Outline each blood parasite and name the species.
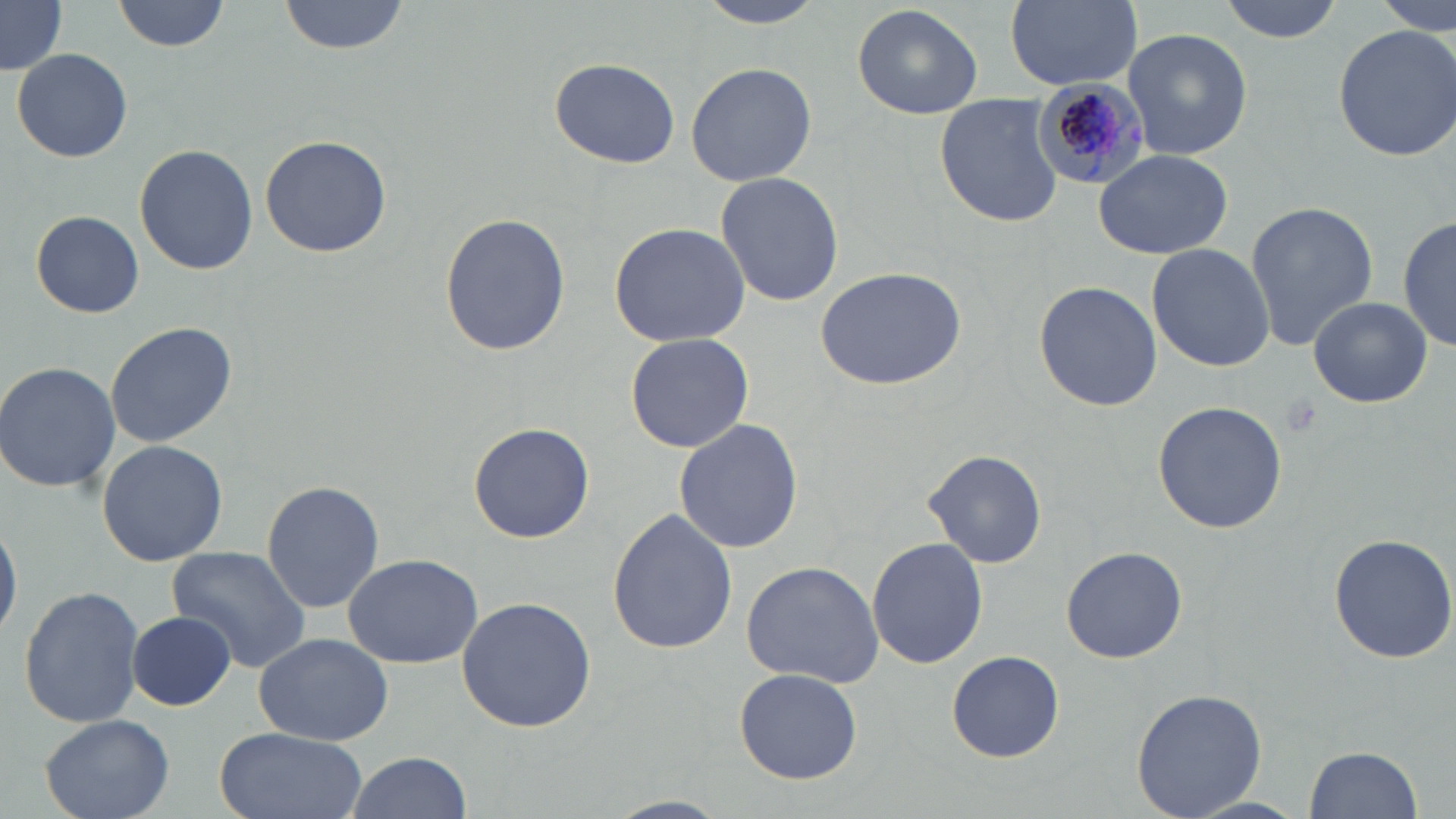

Approximate bounding boxes as [x1, y1, x2, y2] in pixels.
Plasmodium malariae-infected red blood cells: [1028, 80, 1149, 190].
No Plasmodium falciparum, Plasmodium ovale, Plasmodium vivax, Babesia divergens, or Trypanosoma brucei observed.

Summary:
  - Uninfected red blood cell locations: [113, 0, 230, 52], [278, 0, 407, 55], [695, 0, 829, 27], [1005, 0, 1142, 88], [1219, 0, 1347, 43], [1377, 0, 1453, 35], [1, 3, 67, 75], [852, 3, 984, 117], [1333, 21, 1456, 161], [1122, 27, 1253, 161], [12, 48, 133, 164], [550, 56, 681, 168], [685, 59, 817, 186], [935, 99, 1062, 225], [258, 132, 393, 259], [135, 144, 257, 274], [1093, 148, 1234, 260], [715, 172, 843, 306], [1244, 200, 1378, 349], [438, 210, 570, 358], [1399, 210, 1454, 354], [30, 211, 145, 318], [608, 221, 751, 348], [1146, 244, 1275, 371], [814, 266, 967, 391], [1033, 280, 1163, 412], [1308, 296, 1431, 408], [105, 320, 237, 448], [625, 331, 754, 453], [0, 360, 121, 493], [1152, 400, 1287, 536], [673, 418, 804, 553], [468, 423, 594, 543], [96, 439, 228, 567], [923, 448, 1047, 569], [261, 481, 384, 614], [606, 507, 738, 656], [0, 512, 21, 644], [1327, 532, 1456, 664], [867, 536, 989, 669], [1062, 544, 1186, 663], [167, 546, 309, 670], [342, 552, 483, 670], [739, 560, 884, 686], [18, 584, 146, 729], [456, 596, 597, 732], [125, 612, 236, 711], [253, 632, 394, 747], [946, 648, 1067, 762], [734, 667, 861, 784], [1131, 686, 1267, 817], [40, 713, 174, 819], [211, 728, 369, 819], [1303, 745, 1422, 819], [346, 751, 471, 818]
  - Platelet locations: [1277, 394, 1323, 438]
  - Slide-level diagnosis: Plasmodium malariae
  - Magnification: 1000x
  - Stain: May-Grünwald-Giemsa
  - Modality: light microscopy
  - Field of view: one of a larger specimen
  - Image size: 1456×819 pixels
  - Preparation: thin blood film